Give the preparation type.
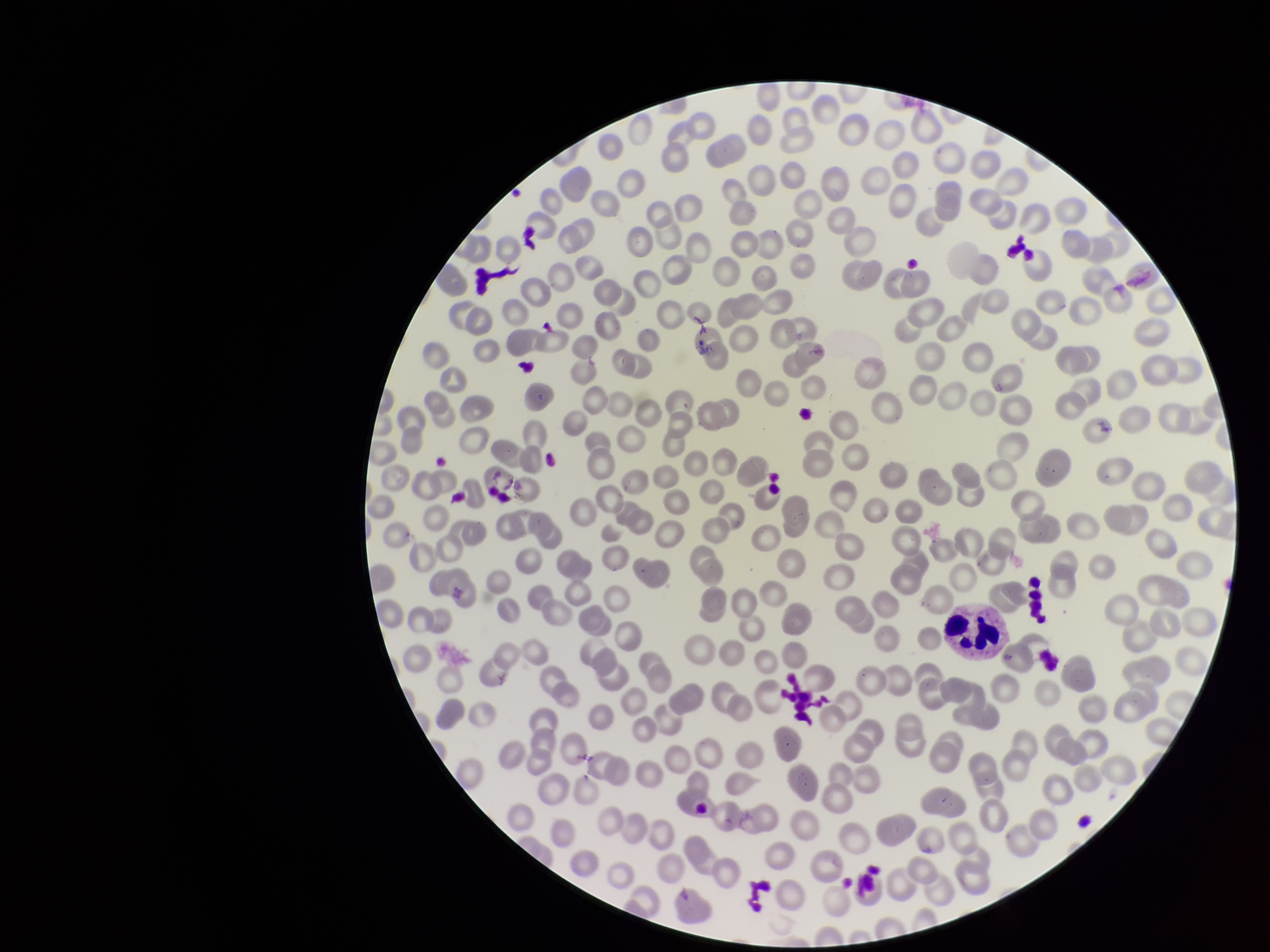

It is a thin blood smear.

Red blood cell count: 254. Patient malaria status: negative. Single field of view. Giemsa stain. Parasitized red blood cell count: 0. Image is 1270×952 pixels. Smartphone photograph taken through the eyepiece of a microscope. Parasitized red blood cells: none detected.